Assess this cell for malaria.
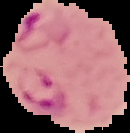
Parasitized.

{
  "preparation": "thin blood smear",
  "image_type": "cell region segmented out of the field of view; surrounding area masked to black",
  "image_size": "130×133 pixels"
}